Report the malaria status of this cell.
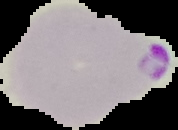

It is parasitized.

image type = segmented cell region with the area outside set to black
image size = 178×130 pixels
preparation = thin blood film